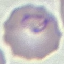 Malaria status: parasitized. Giemsa-stained preparation. Acquired by smartphone through the microscope eyepiece. Automatically extracted cell patch, resized to 64 × 64 pixels. Thin blood film.